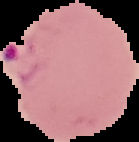
image type = segmented cell region with the area outside set to black
preparation = thin blood film
malaria status = parasitized
image size = 139×142 pixels